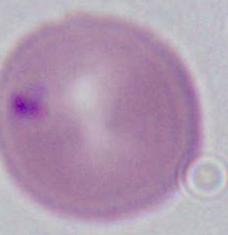

Summary:
  - Magnification: 1000x
  - Identification: erythrocyte
  - Modality: micrograph